Outline each Plasmodium vivax-infected red blood cell.
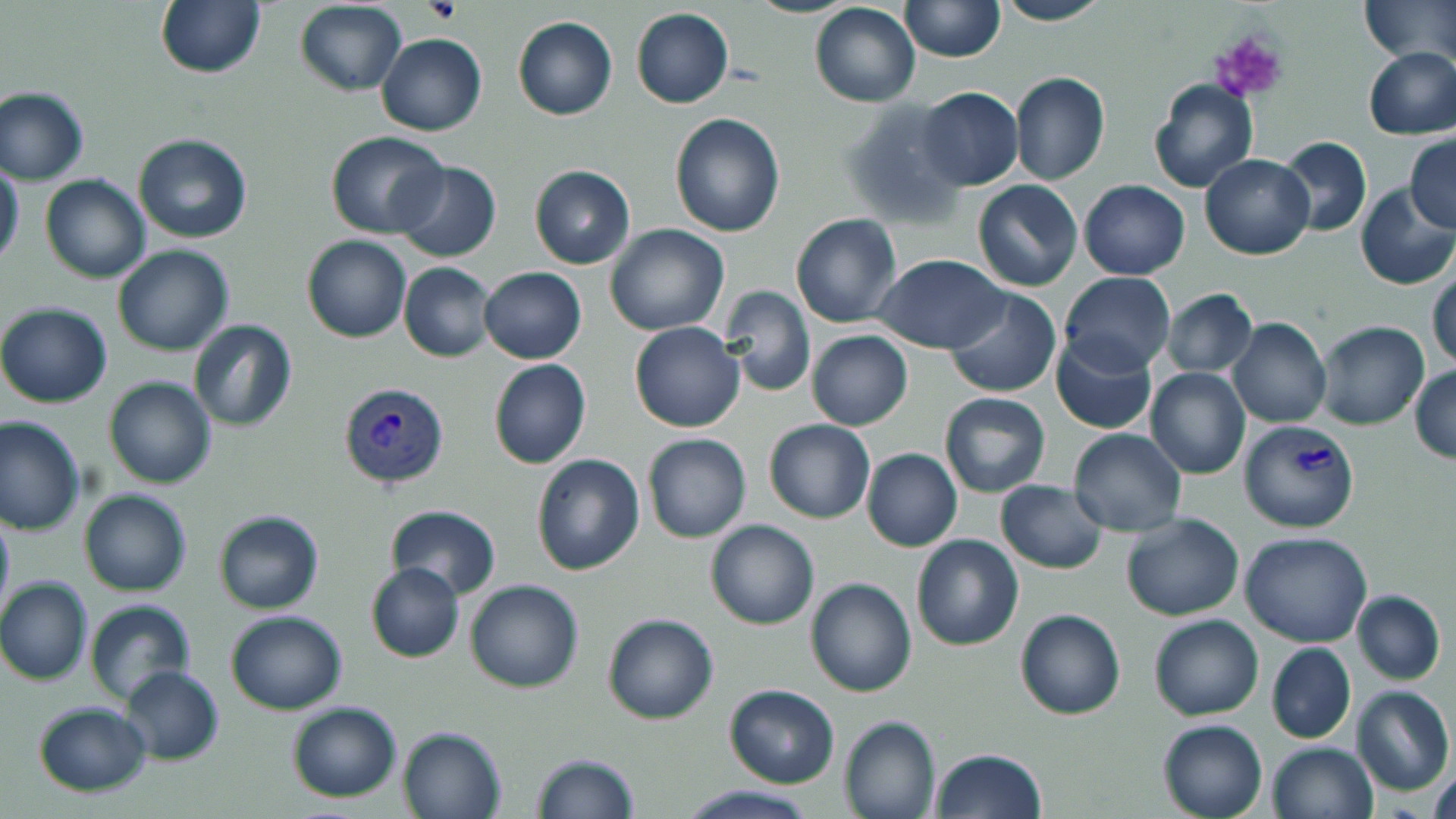

Approximate bounding boxes as (x1,y1)-(x2,y2) corner pairs in pixels.
Plasmodium vivax-infected red blood cells: (343,381)-(454,490), (1237,419)-(1361,535).

Summary:
  - Platelet locations: (424,0)-(460,24), (1206,30)-(1289,103)
  - Uninfected red blood cell locations: (155,0)-(266,80), (994,0)-(1112,26), (900,1)-(1004,64), (1359,1)-(1456,64), (294,2)-(407,95), (809,3)-(920,107), (630,8)-(734,109), (512,15)-(617,120), (376,33)-(487,136), (1363,47)-(1456,138), (1010,72)-(1110,186), (1147,78)-(1259,194), (1,87)-(89,186), (916,87)-(1022,190), (836,98)-(966,229), (669,112)-(786,238), (132,132)-(253,243), (325,132)-(449,239), (1405,135)-(1456,232), (1276,136)-(1372,238), (1200,153)-(1313,260), (393,161)-(502,263), (0,164)-(24,268), (529,165)-(635,268), (39,174)-(150,283), (973,179)-(1083,292), (1079,180)-(1190,280), (1355,184)-(1456,291), (790,212)-(902,328), (604,224)-(729,334), (302,235)-(410,342), (111,245)-(234,356), (873,254)-(1008,353), (399,261)-(497,363), (479,267)-(585,364), (1429,267)-(1456,374), (1060,272)-(1176,374), (719,285)-(816,396), (944,288)-(1062,399), (1160,289)-(1258,378), (0,302)-(112,409), (1228,317)-(1331,429), (188,320)-(300,433), (1315,321)-(1430,431), (629,322)-(745,434), (806,330)-(914,431), (1050,332)-(1158,436), (488,359)-(592,470), (1410,365)-(1455,464), (1146,368)-(1250,480), (103,376)-(215,488), (938,390)-(1050,497), (0,416)-(85,536), (764,419)-(875,523), (1068,429)-(1186,535), (643,432)-(751,543), (861,448)-(963,551), (531,453)-(646,575), (995,480)-(1108,573), (79,489)-(192,596), (387,506)-(502,598), (0,508)-(14,625), (213,509)-(324,614), (1121,513)-(1245,621), (704,519)-(820,629), (1239,531)-(1372,647), (910,534)-(1024,651), (365,562)-(464,663), (804,576)-(918,697), (1,578)-(92,687), (465,578)-(584,693), (1351,590)-(1445,684), (84,598)-(197,705), (1014,607)-(1125,720), (224,609)-(347,713), (601,611)-(719,725), (1149,613)-(1264,722), (1266,642)-(1356,745), (118,665)-(225,765), (723,685)-(840,788), (1352,685)-(1453,798), (285,700)-(403,802), (33,702)-(153,796), (839,715)-(940,819), (1157,718)-(1269,819), (397,726)-(506,818), (1265,742)-(1378,819), (927,748)-(1049,818), (531,752)-(639,819), (1428,757)-(1456,819), (676,784)-(822,819)
  - Slide-level diagnosis: Plasmodium vivax
  - Stain: May-Grünwald-Giemsa
  - Magnification: 1000x
  - Image size: 1456×819 pixels
  - Field of view: single
  - Preparation: thin blood film
  - Modality: optical microscopy